Locate every Plasmodium ovale-infected red blood cell.
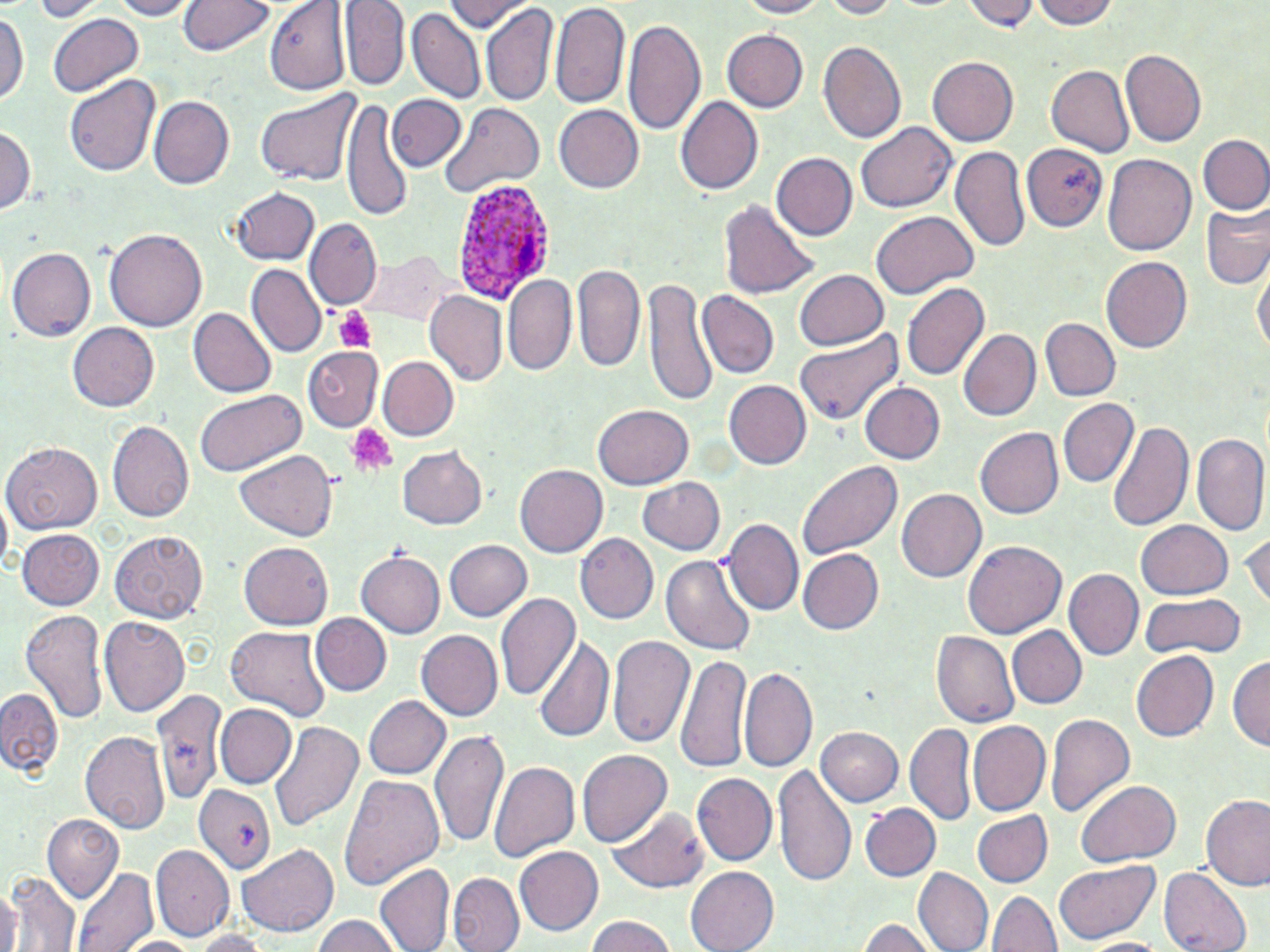
Approximate bounding boxes as named x1/y1/x2/y2 corners in pixels.
Plasmodium ovale-infected red blood cells: (x1=450, y1=177, x2=553, y2=296).

slide_level_diagnosis: Plasmodium ovale
magnification: 1000x
field_of_view: one of a larger specimen
stain: May-Grünwald-Giemsa
uninfected_red_blood_cell_locations: 'approximate bounding boxes as named x1/y1/x2/y2 corners in pixels: (x1=25, y1=0, x2=105, y2=21), (x1=105, y1=0, x2=196, y2=20), (x1=342, y1=0, x2=407, y2=89), (x1=443, y1=0, x2=526, y2=31), (x1=549, y1=0, x2=629, y2=109), (x1=728, y1=0, x2=837, y2=18), (x1=812, y1=0, x2=909, y2=18), (x1=967, y1=0, x2=1037, y2=32), (x1=1031, y1=0, x2=1119, y2=29), (x1=177, y1=1, x2=273, y2=56), (x1=265, y1=2, x2=349, y2=95), (x1=482, y1=4, x2=558, y2=110), (x1=1, y1=11, x2=26, y2=112), (x1=409, y1=12, x2=484, y2=103), (x1=48, y1=13, x2=143, y2=98), (x1=622, y1=16, x2=706, y2=136), (x1=725, y1=30, x2=807, y2=111), (x1=819, y1=42, x2=906, y2=144), (x1=1123, y1=49, x2=1208, y2=147), (x1=928, y1=57, x2=1019, y2=146), (x1=1043, y1=64, x2=1131, y2=155), (x1=65, y1=75, x2=161, y2=178), (x1=256, y1=88, x2=363, y2=188), (x1=387, y1=95, x2=464, y2=172), (x1=677, y1=97, x2=763, y2=196), (x1=150, y1=98, x2=234, y2=188), (x1=342, y1=100, x2=410, y2=219), (x1=440, y1=103, x2=544, y2=198), (x1=551, y1=104, x2=644, y2=193), (x1=856, y1=121, x2=955, y2=213), (x1=2, y1=124, x2=35, y2=221), (x1=1198, y1=134, x2=1270, y2=215), (x1=1022, y1=145, x2=1109, y2=229), (x1=952, y1=146, x2=1029, y2=255), (x1=772, y1=153, x2=858, y2=241), (x1=1101, y1=153, x2=1196, y2=257), (x1=232, y1=189, x2=317, y2=264), (x1=721, y1=199, x2=818, y2=301), (x1=1201, y1=205, x2=1270, y2=290), (x1=871, y1=210, x2=979, y2=297), (x1=305, y1=220, x2=381, y2=310), (x1=105, y1=230, x2=208, y2=333), (x1=8, y1=248, x2=95, y2=339), (x1=358, y1=249, x2=456, y2=326), (x1=1101, y1=257, x2=1193, y2=352), (x1=1253, y1=258, x2=1268, y2=366), (x1=573, y1=262, x2=647, y2=374), (x1=249, y1=265, x2=326, y2=356), (x1=794, y1=268, x2=891, y2=351), (x1=503, y1=276, x2=577, y2=375), (x1=643, y1=281, x2=715, y2=405), (x1=900, y1=282, x2=990, y2=382), (x1=695, y1=290, x2=777, y2=379), (x1=423, y1=292, x2=507, y2=388), (x1=189, y1=310, x2=275, y2=397), (x1=1042, y1=318, x2=1121, y2=401), (x1=67, y1=323, x2=162, y2=412), (x1=796, y1=328, x2=904, y2=426), (x1=959, y1=329, x2=1040, y2=422), (x1=305, y1=348, x2=382, y2=430), (x1=378, y1=356, x2=458, y2=439), (x1=723, y1=380, x2=813, y2=469), (x1=858, y1=384, x2=944, y2=465), (x1=193, y1=388, x2=306, y2=475), (x1=1058, y1=398, x2=1138, y2=487), (x1=594, y1=405, x2=693, y2=490), (x1=107, y1=421, x2=194, y2=526), (x1=1109, y1=421, x2=1192, y2=534), (x1=975, y1=426, x2=1064, y2=519), (x1=1193, y1=431, x2=1270, y2=541), (x1=6, y1=443, x2=102, y2=535), (x1=395, y1=446, x2=489, y2=531), (x1=235, y1=449, x2=339, y2=540), (x1=798, y1=460, x2=903, y2=561), (x1=515, y1=464, x2=607, y2=557), (x1=635, y1=477, x2=725, y2=557), (x1=897, y1=489, x2=986, y2=583), (x1=728, y1=519, x2=803, y2=614), (x1=1137, y1=519, x2=1233, y2=598), (x1=17, y1=528, x2=105, y2=610), (x1=111, y1=531, x2=212, y2=621), (x1=1242, y1=532, x2=1269, y2=611), (x1=574, y1=533, x2=657, y2=626), (x1=444, y1=540, x2=531, y2=621), (x1=963, y1=541, x2=1067, y2=639), (x1=239, y1=542, x2=333, y2=628), (x1=796, y1=548, x2=883, y2=637), (x1=357, y1=550, x2=445, y2=640), (x1=662, y1=555, x2=756, y2=656), (x1=1064, y1=569, x2=1144, y2=660), (x1=1140, y1=592, x2=1245, y2=660), (x1=495, y1=593, x2=582, y2=704), (x1=22, y1=609, x2=109, y2=726), (x1=314, y1=614, x2=389, y2=694), (x1=99, y1=617, x2=191, y2=717), (x1=226, y1=625, x2=329, y2=721), (x1=1008, y1=628, x2=1088, y2=709), (x1=417, y1=630, x2=503, y2=720), (x1=932, y1=630, x2=1020, y2=730), (x1=608, y1=633, x2=693, y2=748), (x1=534, y1=636, x2=614, y2=742), (x1=1132, y1=652, x2=1218, y2=741), (x1=675, y1=654, x2=752, y2=772), (x1=1229, y1=654, x2=1269, y2=754), (x1=738, y1=666, x2=816, y2=772), (x1=0, y1=685, x2=65, y2=777), (x1=158, y1=694, x2=223, y2=806), (x1=362, y1=694, x2=451, y2=780), (x1=218, y1=703, x2=295, y2=787), (x1=1047, y1=714, x2=1134, y2=820), (x1=269, y1=720, x2=365, y2=831), (x1=907, y1=720, x2=974, y2=827), (x1=967, y1=721, x2=1050, y2=818), (x1=816, y1=726, x2=906, y2=808), (x1=431, y1=728, x2=509, y2=848), (x1=82, y1=732, x2=173, y2=832), (x1=578, y1=747, x2=675, y2=846), (x1=488, y1=760, x2=579, y2=865), (x1=776, y1=763, x2=855, y2=887), (x1=340, y1=773, x2=443, y2=893), (x1=692, y1=774, x2=777, y2=866), (x1=1075, y1=779, x2=1181, y2=865), (x1=194, y1=784, x2=275, y2=873), (x1=1202, y1=796, x2=1270, y2=889), (x1=609, y1=804, x2=709, y2=893), (x1=859, y1=804, x2=939, y2=882), (x1=973, y1=810, x2=1052, y2=887), (x1=43, y1=815, x2=124, y2=901), (x1=236, y1=843, x2=340, y2=938), (x1=152, y1=845, x2=234, y2=939), (x1=515, y1=847, x2=605, y2=936), (x1=1052, y1=857, x2=1163, y2=944), (x1=1159, y1=865, x2=1250, y2=952), (x1=73, y1=866, x2=157, y2=952), (x1=377, y1=866, x2=454, y2=951), (x1=686, y1=868, x2=778, y2=952), (x1=916, y1=870, x2=992, y2=951), (x1=9, y1=871, x2=80, y2=951), (x1=448, y1=871, x2=524, y2=952), (x1=0, y1=880, x2=20, y2=952), (x1=987, y1=890, x2=1062, y2=952), (x1=310, y1=914, x2=406, y2=952), (x1=582, y1=915, x2=681, y2=952), (x1=858, y1=916, x2=937, y2=952), (x1=187, y1=929, x2=274, y2=952), (x1=115, y1=934, x2=204, y2=952), (x1=1077, y1=935, x2=1175, y2=951)'
image_size: 1270×952 pixels
modality: light microscopy
platelet_locations: 'approximate bounding boxes as named x1/y1/x2/y2 corners in pixels: (x1=334, y1=307, x2=375, y2=353), (x1=345, y1=425, x2=395, y2=477)'
preparation: thin blood smear